Classify this cell by malaria status.
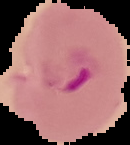
It is parasitized.

Summary:
  - Image size: 130×145 pixels
  - Image type: segmented cell region on a black background
  - Preparation: thin blood smear